Point out every malaria parasite.
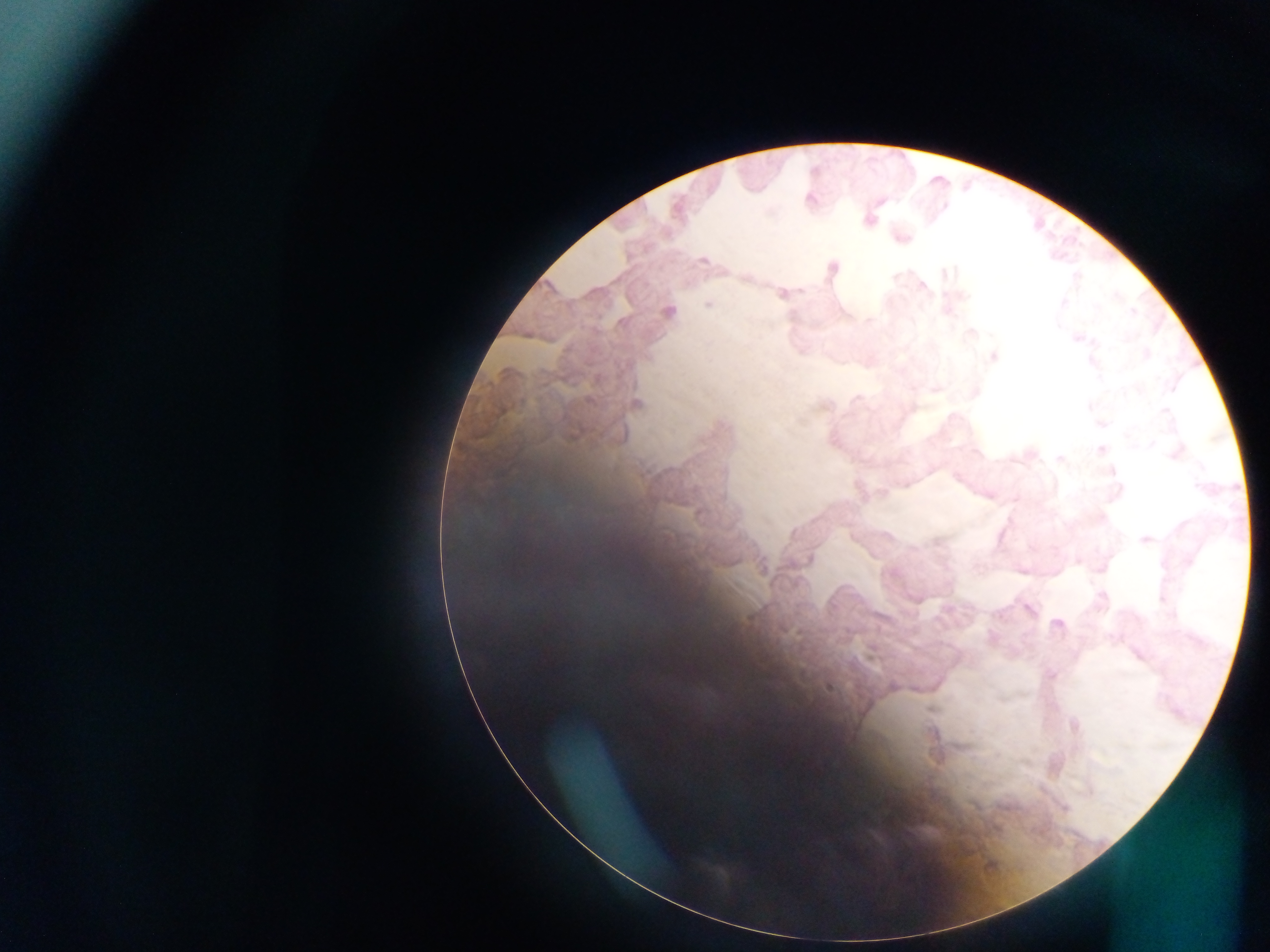
Approximate centers as {x, y} in pixels.
Malaria parasites: {1063, 303}, {708, 304}, {1101, 449}, {1056, 624}.

Thick blood film. Sample from Ghana. Single field of view. Photographed through a microscope with a mobile-phone camera. Image is 1270×952 pixels.